Report the malaria status of this cell.
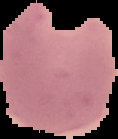

Parasitized.

Image is 118×139 pixels. The area outside the segmented cell region is set to black. From a thin blood smear.